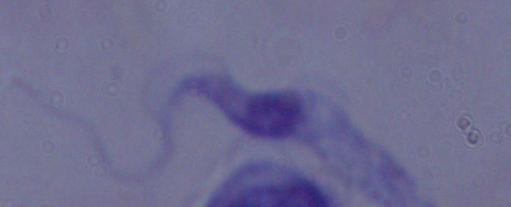

Summary:
  - Identification: trypanosome
  - Magnification: 1000x
  - Modality: micrograph